State the preparation type.
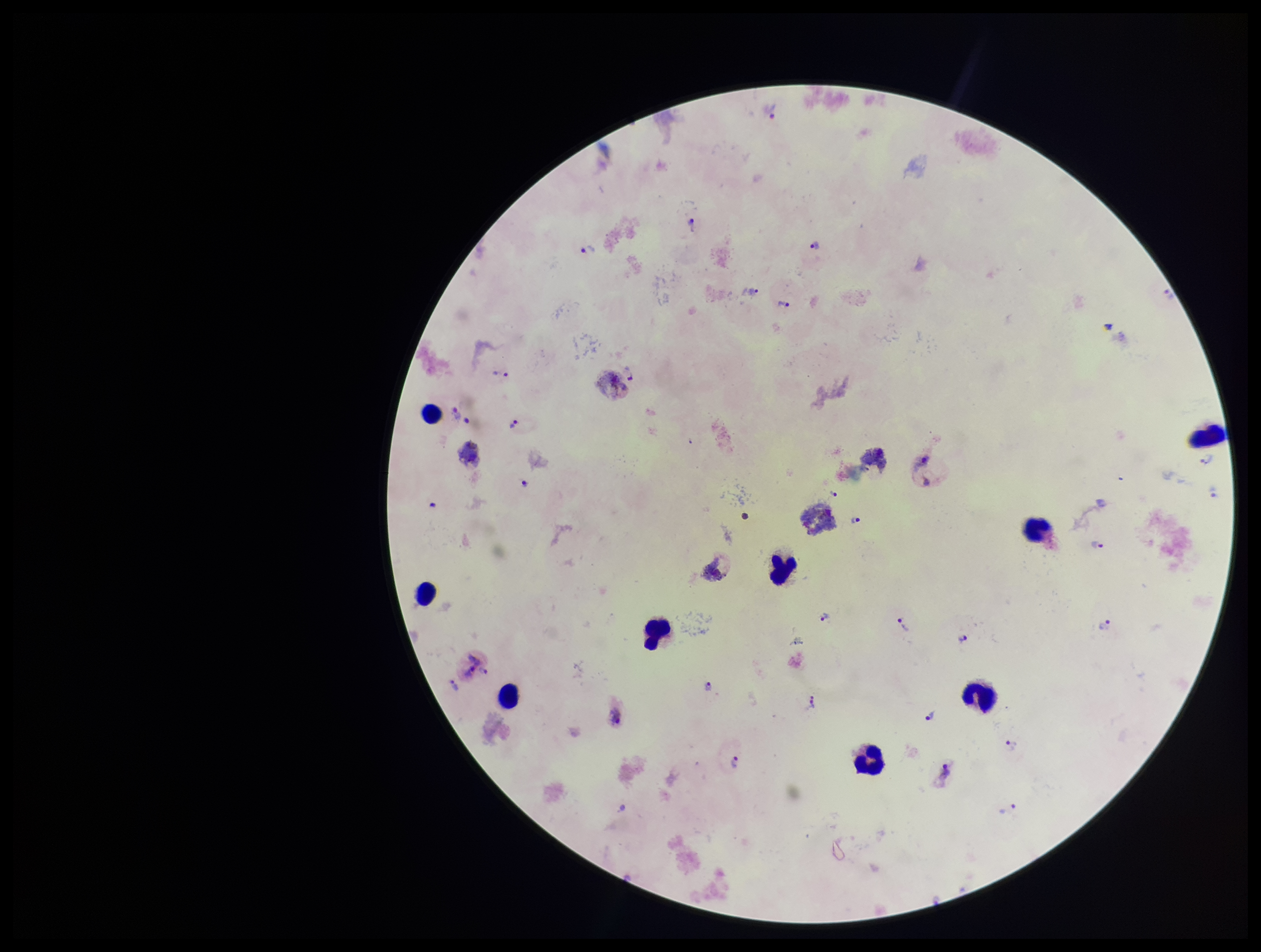

Thick.

Summary:
  - Stain: Giemsa
  - Parasite count: 26
  - Image size: 1261×952 pixels
  - Capture: smartphone photograph through the microscope eyepiece
  - Patient malaria status: positive
  - Species reported for this patient: Plasmodium vivax
  - Leukocyte count: 9
  - Field of view: one from this slide
  - Plasmodium parasites: identified